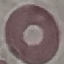

Summary:
  - Result: negative for malaria parasites
  - Capture: smartphone camera at the microscope eyepiece
  - Preparation: thin blood smear
  - Image type: cell patch, automatically extracted from a larger field of view and resized to 64 × 64 pixels
  - Stain: Giemsa